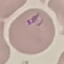

Summary:
  - Result: malaria parasites detected
  - Capture: smartphone camera at the microscope eyepiece
  - Image type: automatically extracted cell patch, resized to 64 × 64 pixels
  - Preparation: thin blood film
  - Stain: Giemsa